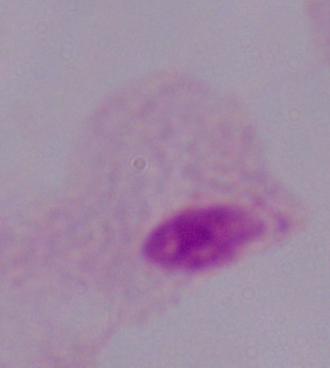
modality = micrograph
magnification = 1000x
identification = trichomonad